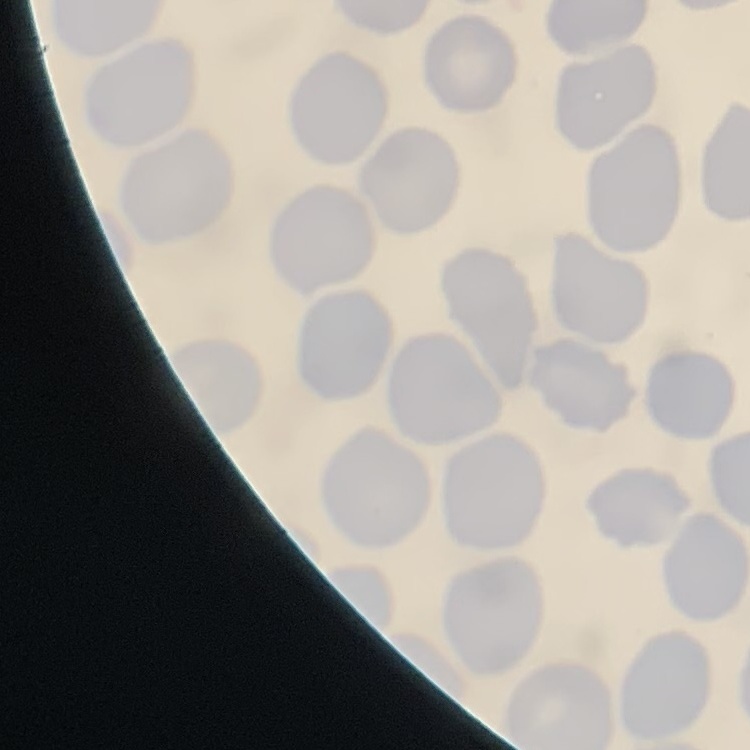 The red blood cells exhibit no rouleaux formation. Square crop of a larger photomicrograph. Thin peripheral smear. Field's or Giemsa stain.